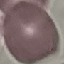

Summary:
  - Malaria status: uninfected
  - Image type: cell patch, automatically extracted from a larger field of view and resized to 64 × 64 pixels
  - Preparation: thin blood film
  - Stain: Giemsa
  - Capture: smartphone through the microscope eyepiece